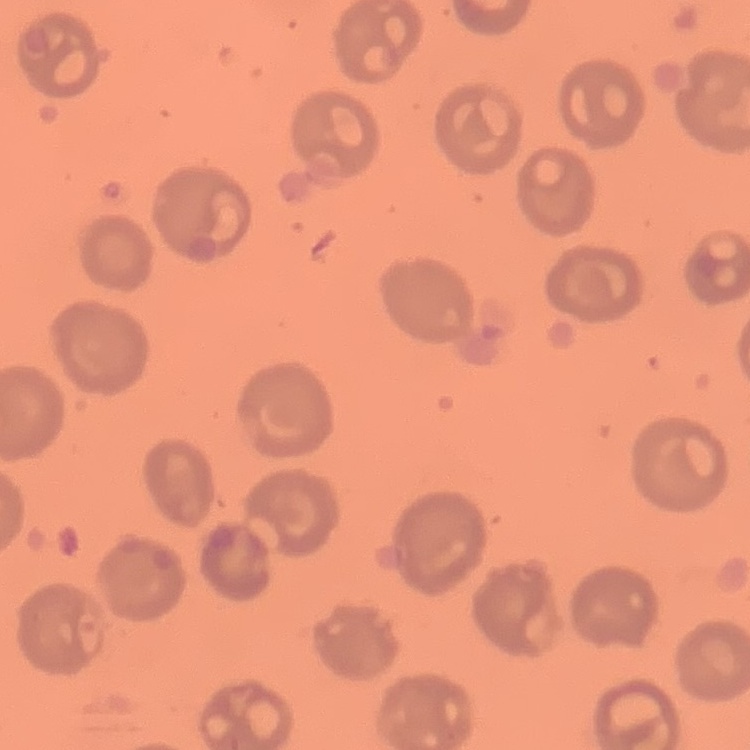
Summary:
  - Red blood cell morphology: no rouleaux formation
  - Preparation: thin blood film
  - Image type: square crop of a larger photomicrograph
  - Stain: Field's or Giemsa